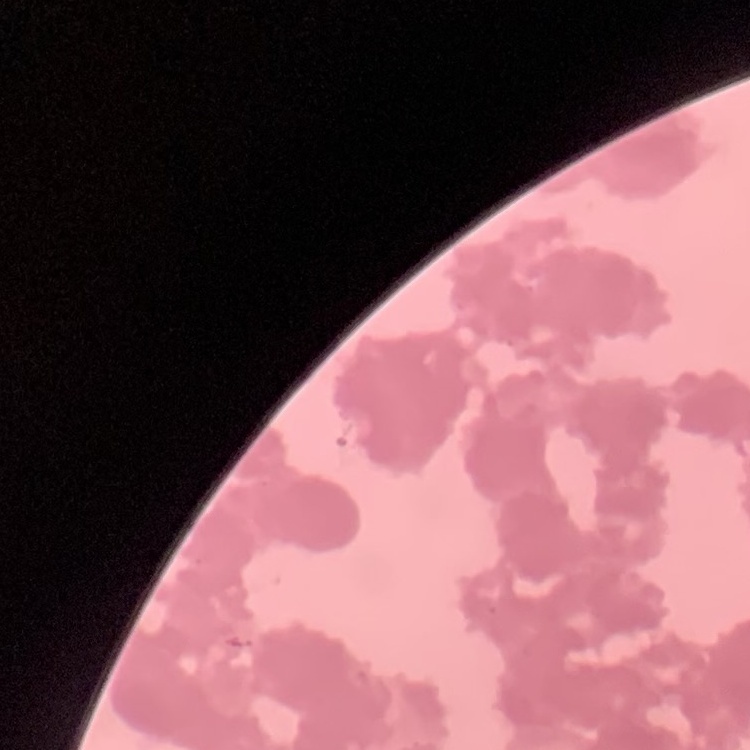
erythrocyte morphology = rouleaux formation
image type = square crop of a larger photomicrograph
preparation = thin blood film
stain = Field's or Giemsa